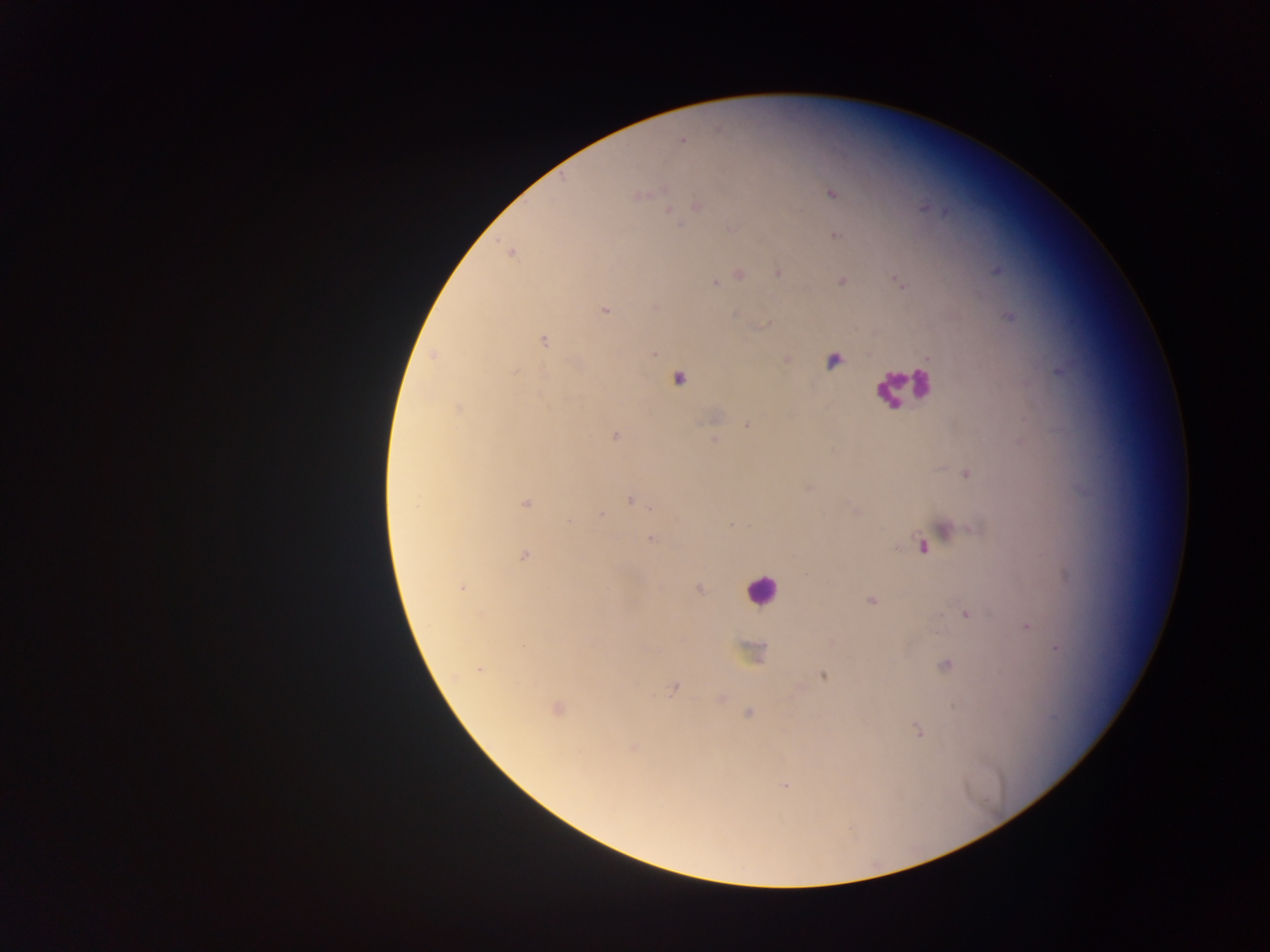
image size = 1270×952 pixels
capture = mobile-phone photograph through a microscope
preparation = thick blood film
field of view = single
Plasmodium parasite locations = approximate centers as [x, y] in pixels: [680, 142], [660, 191], [828, 193], [638, 195], [697, 205], [669, 210], [833, 234], [778, 273], [739, 274], [841, 280], [717, 282], [606, 310], [738, 312], [1009, 316], [763, 324], [543, 340], [655, 351], [431, 356], [834, 360], [515, 372], [678, 378], [458, 406], [747, 423], [614, 435], [714, 438], [967, 473], [808, 486], [630, 500], [527, 503], [414, 505], [650, 508], [600, 513], [567, 520], [947, 528], [653, 537], [922, 544], [525, 555], [1067, 574], [463, 588], [699, 589], [870, 600], [964, 612], [1026, 625], [1057, 646], [744, 653], [945, 663], [479, 669], [821, 676], [673, 688], [721, 698], [953, 705], [558, 709], [747, 714], [917, 730], [630, 748], [786, 785]
leukocyte locations = approximate centers as [x, y] in pixels: [895, 386], [761, 594]
country = Ghana